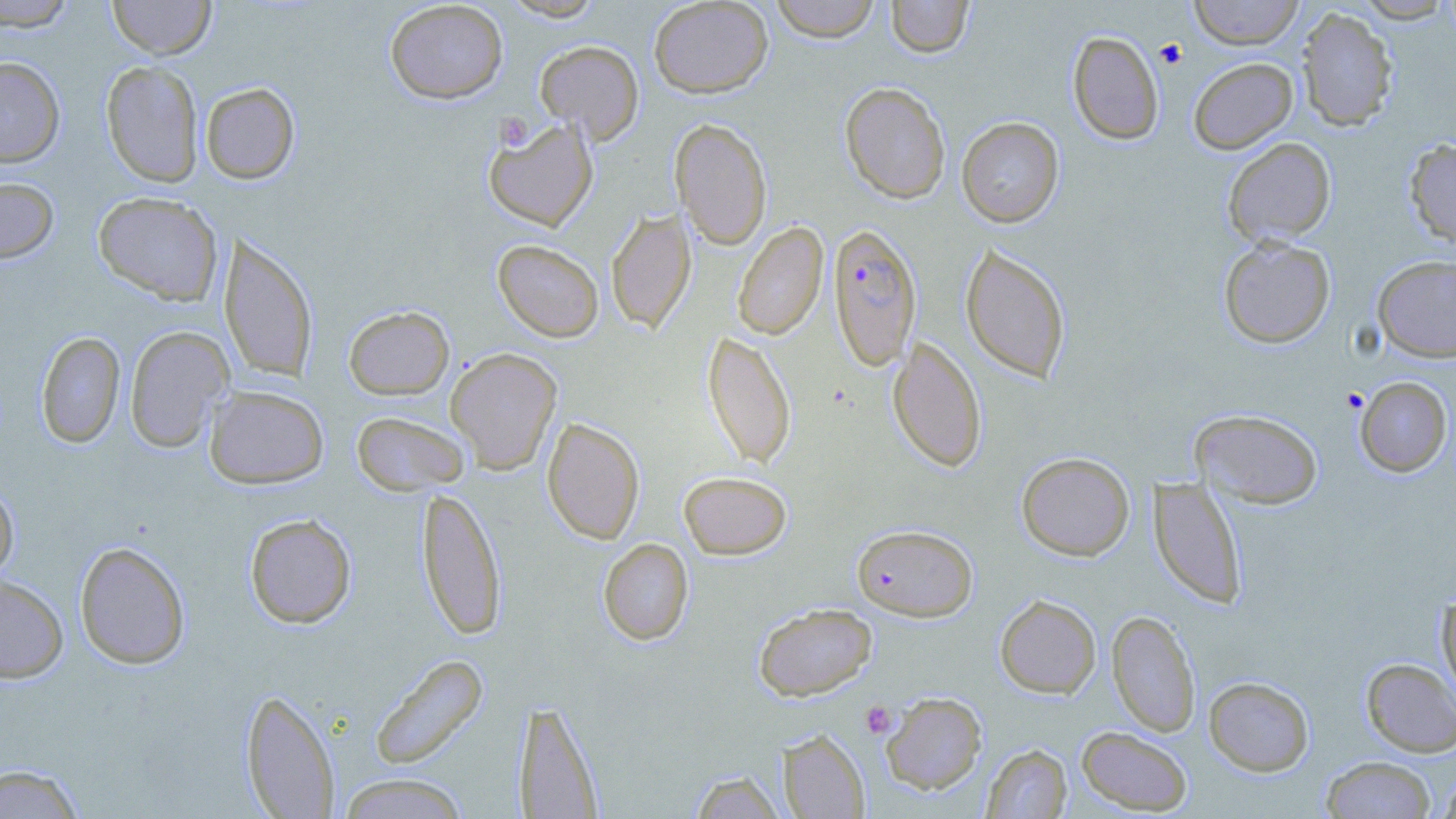

Approximate bounding boxes as [x1, y1, x2, y2] in pixels. Platelet locations: [1155, 39, 1187, 68], [861, 701, 896, 738]. Uninfected red blood cell locations (subset): [108, 0, 215, 59], [384, 0, 508, 104], [501, 0, 606, 22], [649, 0, 773, 98], [769, 0, 881, 42], [885, 0, 975, 58], [1187, 0, 1305, 49], [1351, 0, 1455, 23], [0, 1, 78, 31], [1296, 8, 1399, 131], [1067, 30, 1164, 144], [535, 40, 644, 143], [0, 57, 65, 167], [1188, 57, 1298, 154], [101, 60, 204, 187], [200, 82, 299, 184], [840, 82, 951, 204], [482, 116, 599, 231], [956, 117, 1064, 228], [670, 118, 772, 249], [1222, 137, 1336, 246], [1404, 138, 1456, 248], [0, 176, 59, 264], [93, 191, 224, 306], [605, 208, 696, 333], [733, 222, 828, 340], [219, 233, 318, 383], [1218, 236, 1336, 348], [493, 240, 604, 342], [960, 242, 1071, 383], [1372, 255, 1456, 363], [343, 305, 454, 400], [125, 325, 233, 452], [702, 330, 796, 469], [35, 332, 125, 449], [888, 337, 987, 472], [445, 347, 563, 474], [1354, 376, 1453, 477], [204, 385, 329, 489], [1191, 409, 1323, 509], [352, 411, 470, 496], [542, 417, 645, 544], [1016, 451, 1135, 561], [679, 471, 792, 559], [1148, 477, 1249, 608], [0, 478, 19, 583], [417, 487, 507, 640], [244, 513, 357, 629], [598, 538, 694, 645], [74, 540, 191, 670], [0, 573, 68, 683], [1436, 593, 1456, 708], [994, 594, 1101, 698], [753, 602, 877, 701], [1107, 610, 1200, 738], [369, 653, 488, 770], [1361, 657, 1456, 757], [1204, 675, 1314, 776], [241, 688, 340, 818], [880, 691, 987, 795], [514, 698, 605, 817], [1076, 726, 1193, 815], [779, 729, 870, 818], [982, 743, 1072, 818], [1321, 756, 1436, 818], [0, 763, 86, 818], [1435, 769, 1456, 819], [688, 770, 786, 818], [337, 773, 470, 818]. Plasmodium falciparum-infected red blood cell locations (subset): [827, 223, 922, 371]. Slide-level diagnosis: Plasmodium falciparum. Captured at 1000x magnification. Thin blood film. May-Grünwald-Giemsa stain. Optical microscopy. One field of a larger specimen. Image is 1456×819 pixels.